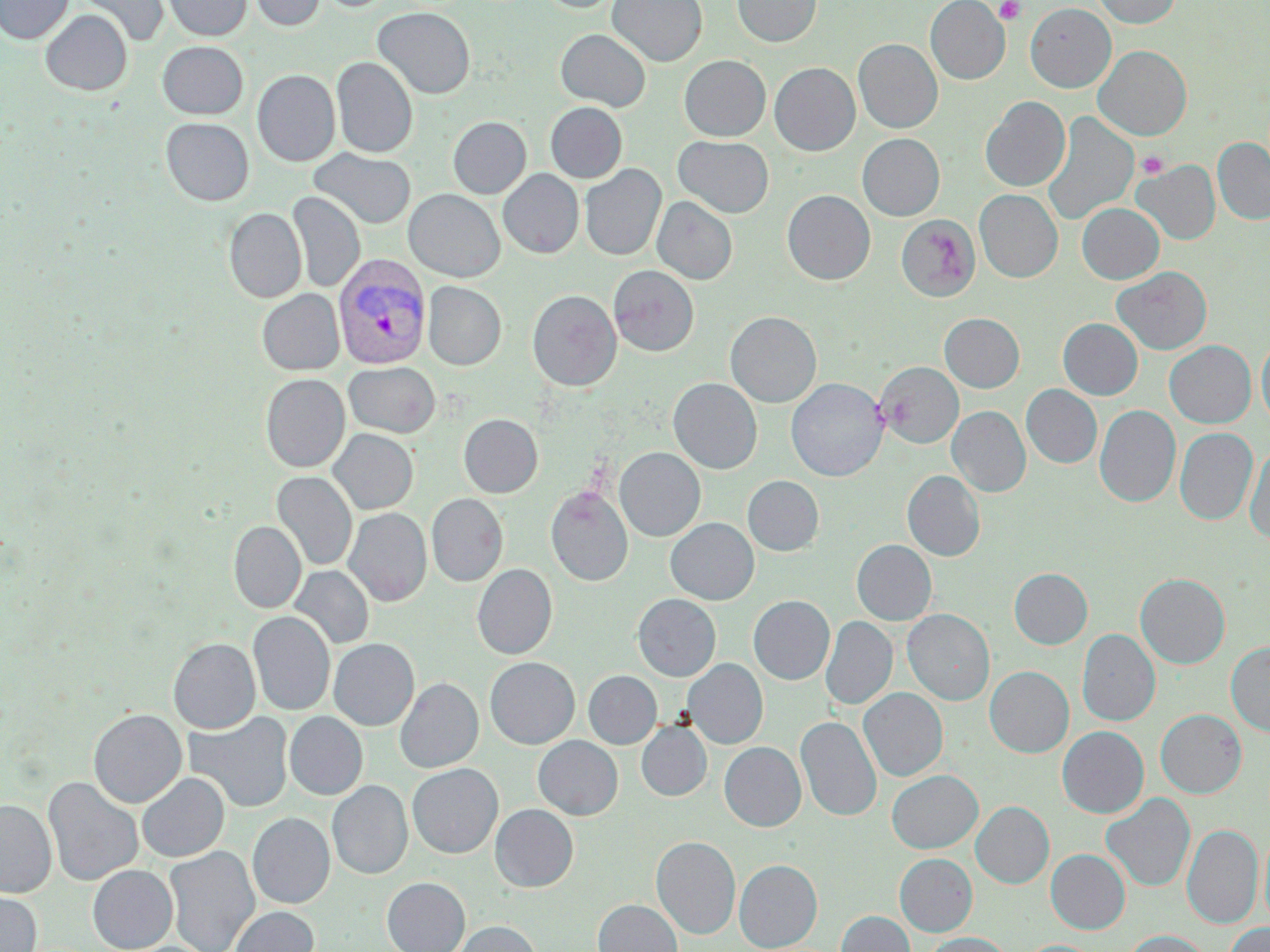
Summary:
  - Coordinate format: approximate bounding boxes as (x1,y1)-(x2,y2) corner pairs in pixels
  - Platelet locations: (995,1)-(1027,24), (1136,151)-(1169,178)
  - Plasmodium vivax-infected red blood cell locations: (333,254)-(431,369)
  - Uninfected red blood cell locations: (0,0)-(73,43), (74,0)-(169,48), (163,0)-(252,41), (249,0)-(326,31), (537,0)-(624,12), (608,0)-(706,66), (732,0)-(821,47), (926,0)-(1009,84), (1092,0)-(1181,28), (1025,3)-(1116,92), (373,6)-(475,99), (40,9)-(132,95), (555,29)-(651,111), (853,39)-(942,133), (158,41)-(248,119), (1094,45)-(1191,140), (679,55)-(770,141), (331,57)-(418,158), (770,63)-(860,155), (252,69)-(341,166), (980,96)-(1070,191), (545,102)-(627,183), (1042,112)-(1138,226), (448,116)-(531,198), (161,118)-(254,205), (857,133)-(945,220), (673,136)-(774,217), (1212,138)-(1270,225), (309,148)-(416,230), (1134,160)-(1220,245), (580,164)-(666,260), (498,169)-(583,258), (404,189)-(505,281), (975,189)-(1062,282), (782,190)-(875,284), (288,191)-(365,292), (652,196)-(737,284), (1077,203)-(1164,284), (224,208)-(306,303), (896,214)-(980,301), (609,265)-(699,356), (1112,266)-(1212,355), (423,281)-(505,370), (257,289)-(344,375), (527,290)-(621,391), (725,311)-(821,407), (940,313)-(1024,392), (1058,318)-(1143,399), (1256,335)-(1270,428), (1164,341)-(1256,427), (344,362)-(440,438), (876,362)-(963,448), (261,374)-(350,472), (669,378)-(762,474), (786,378)-(888,481), (1021,385)-(1101,468), (1095,405)-(1181,508), (947,406)-(1030,497), (458,413)-(543,497), (1175,427)-(1257,525), (329,429)-(418,515), (1245,443)-(1270,545), (614,447)-(705,541), (903,470)-(985,561), (272,471)-(357,571), (743,475)-(824,556), (545,486)-(633,586), (427,493)-(508,587), (344,508)-(431,606), (665,518)-(758,604), (229,521)-(306,613), (852,540)-(936,625), (472,564)-(557,659), (289,566)-(374,650), (479,566)-(564,749), (1009,568)-(1092,649), (1136,573)-(1230,669), (633,594)-(720,681), (748,595)-(834,684), (903,609)-(994,705), (248,611)-(335,715), (821,616)-(897,710), (1077,629)-(1160,727), (168,638)-(260,733), (329,638)-(419,730), (1226,642)-(1270,736), (485,657)-(580,749), (683,659)-(767,748), (985,666)-(1073,757), (584,671)-(661,748), (395,677)-(483,773), (859,688)-(947,781), (88,709)-(186,808), (1156,709)-(1246,797), (284,711)-(367,800), (184,712)-(294,813), (796,716)-(881,820), (637,721)-(711,800), (1058,726)-(1148,818), (533,736)-(622,819), (720,742)-(805,831), (407,763)-(503,858), (887,770)-(982,853), (137,773)-(229,862), (43,776)-(143,887), (327,780)-(412,879), (1101,793)-(1195,892), (0,799)-(56,897), (971,801)-(1054,888), (490,804)-(578,892), (248,812)-(334,908), (1182,824)-(1262,928), (1259,829)-(1270,931), (651,836)-(740,939), (164,846)-(259,952), (1046,849)-(1130,934), (895,853)-(977,936), (734,860)-(822,951), (88,865)-(177,951), (382,877)-(470,952), (0,890)-(41,952), (593,899)-(682,952), (230,906)-(319,952), (836,911)-(915,952), (452,921)-(540,952), (1225,923)-(1270,952), (1122,931)-(1212,952), (922,933)-(1011,952), (1019,940)-(1100,952)
  - Slide-level diagnosis: Plasmodium vivax
  - Field of view: single
  - Image size: 1270×952 pixels
  - Preparation: thin blood smear
  - Magnification: 1000x
  - Stain: May-Grünwald-Giemsa
  - Modality: light microscopy